Report the malaria status of this cell.
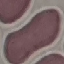
Uninfected.

Thin blood film. Acquired by smartphone through the microscope eyepiece. Automatically extracted cell patch, resized to 64 × 64 pixels. Giemsa stain.